Classify this cell by malaria status.
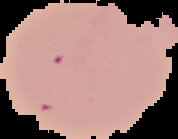

It is uninfected.

image_type: cell region segmented out of the field of view; surrounding area masked to black
preparation: thin blood smear
image_size: 178×139 pixels